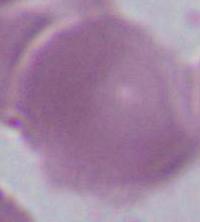

magnification = 1000x
modality = photomicrograph
identification = red blood cell